Assess the morphology of the red blood cells.
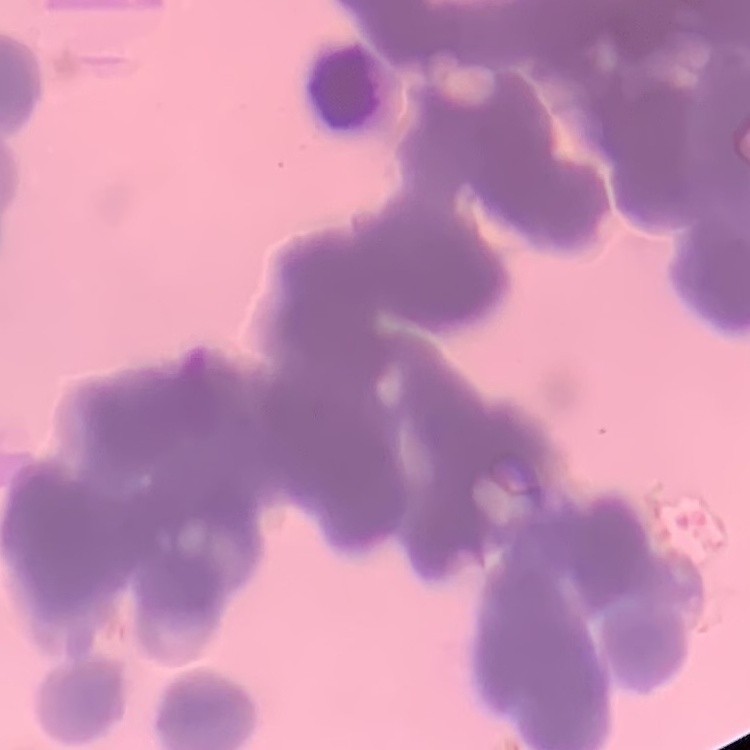

Rouleaux formation.

Square crop of a larger photomicrograph. Stained with either Field's or Giemsa. Thin blood film.